State which parasite is depicted.
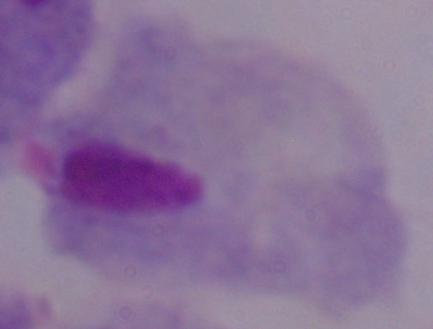

This is a trichomonad.

Photomicrograph. 1000x magnification.